Classify this cell by malaria status.
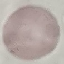
Uninfected.

Summary:
  - Capture: smartphone camera at the microscope eyepiece
  - Stain: Giemsa
  - Preparation: thin blood film
  - Image type: cell patch, automatically extracted from a larger field of view and resized to 64 × 64 pixels